Locate every blood parasite and identify its species.
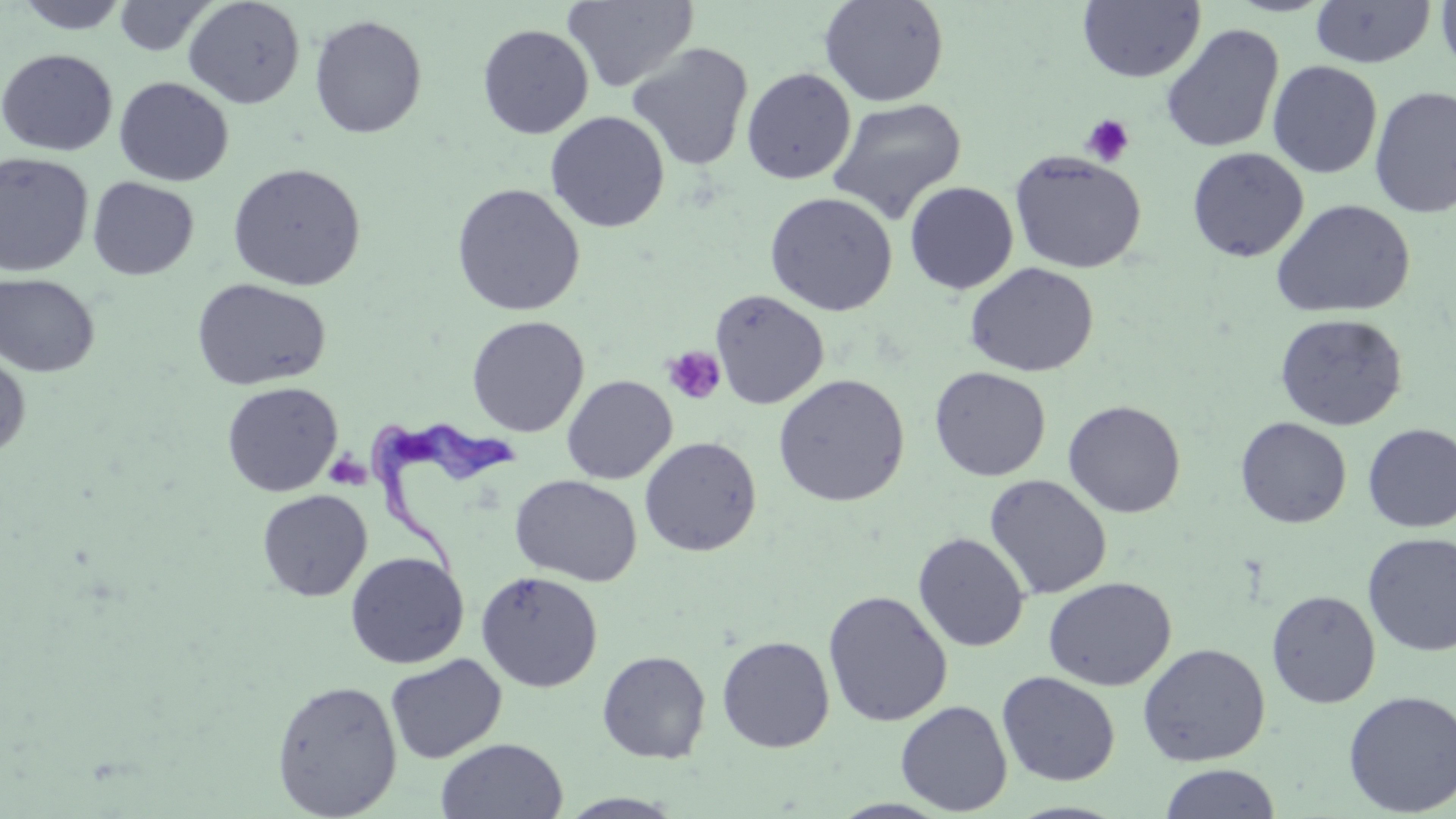

Approximate bounding boxes as [x1, y1, x2, y2] in pixels.
Trypanosoma brucei: [367, 415, 520, 578].
No Plasmodium falciparum, Plasmodium ovale, Plasmodium malariae, Plasmodium vivax, or Babesia divergens observed.

slide-level diagnosis = Trypanosoma brucei
platelet locations = approximate bounding boxes as [x1, y1, x2, y2] in pixels: [1081, 114, 1135, 167], [662, 345, 727, 405]
modality = optical microscopy
uninfected red blood cell locations = approximate bounding boxes as [x1, y1, x2, y2] in pixels: [12, 0, 133, 33], [113, 0, 217, 57], [182, 0, 306, 109], [562, 0, 699, 93], [819, 0, 950, 107], [1436, 0, 1456, 77], [1077, 1, 1206, 83], [1309, 1, 1436, 69], [309, 15, 427, 139], [1160, 23, 1284, 154], [477, 24, 593, 139], [627, 42, 754, 171], [0, 49, 118, 156], [1267, 60, 1382, 178], [741, 68, 856, 184], [114, 78, 234, 186], [1369, 86, 1456, 218], [827, 97, 966, 224], [545, 111, 670, 233], [1186, 147, 1309, 262], [1009, 150, 1146, 274], [0, 152, 94, 277], [227, 162, 366, 291], [88, 177, 199, 280], [904, 181, 1019, 294], [451, 183, 586, 317], [764, 191, 898, 316], [1272, 198, 1415, 319], [964, 262, 1099, 377], [0, 273, 100, 376], [191, 278, 332, 391], [710, 289, 830, 409], [1274, 313, 1408, 431], [466, 315, 589, 437], [0, 349, 32, 460], [929, 366, 1051, 481], [773, 374, 910, 507], [562, 375, 677, 485], [221, 381, 342, 497], [1062, 400, 1186, 518], [1235, 417, 1352, 528], [1362, 423, 1456, 532], [639, 436, 762, 557], [510, 473, 642, 586], [984, 474, 1112, 600], [257, 489, 373, 601], [913, 532, 1030, 652], [1362, 533, 1456, 656], [345, 552, 469, 669], [476, 570, 603, 692], [1043, 576, 1177, 691], [822, 590, 953, 727], [1266, 590, 1380, 708], [717, 635, 835, 752], [1137, 643, 1271, 767], [597, 650, 711, 764], [384, 654, 507, 764], [997, 671, 1120, 786], [270, 679, 402, 818], [1342, 689, 1456, 816], [895, 699, 1013, 815], [435, 738, 568, 819], [1158, 763, 1282, 819], [557, 792, 687, 818]
image size = 1456×819 pixels
stain = May-Grünwald-Giemsa
field of view = single
magnification = 1000x
preparation = thin blood smear